Assess this cell for malaria.
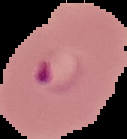
It is parasitized.

Cell region segmented out of the field of view; the surrounding area is masked to black. Image is 127×139 pixels. From a thin blood film.